Describe the morphology of the red blood cells.
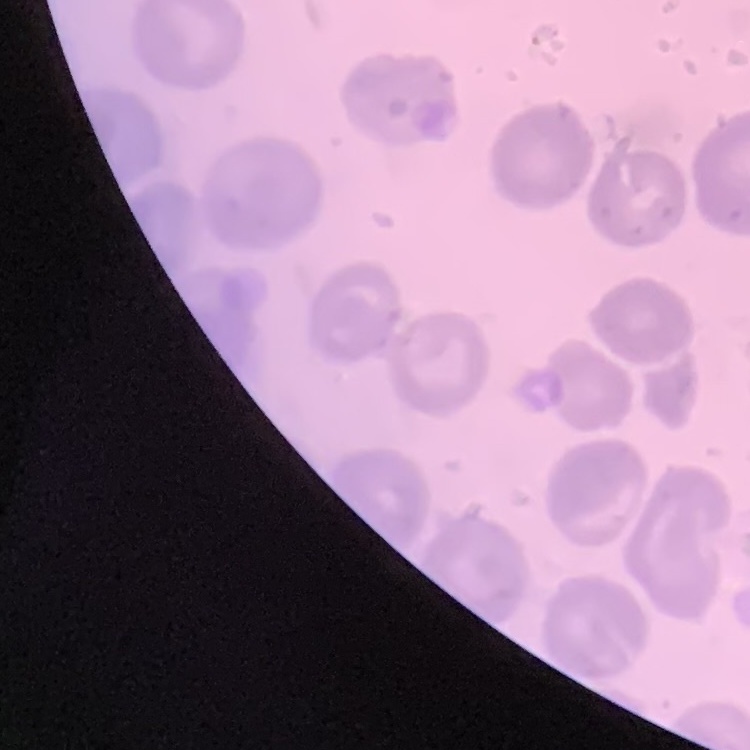
No rouleaux formation.

stain = Field's or Giemsa
preparation = thin blood smear
image type = one tile cut from a larger photomicrograph